Outline each Babesia divergens-infected red blood cell.
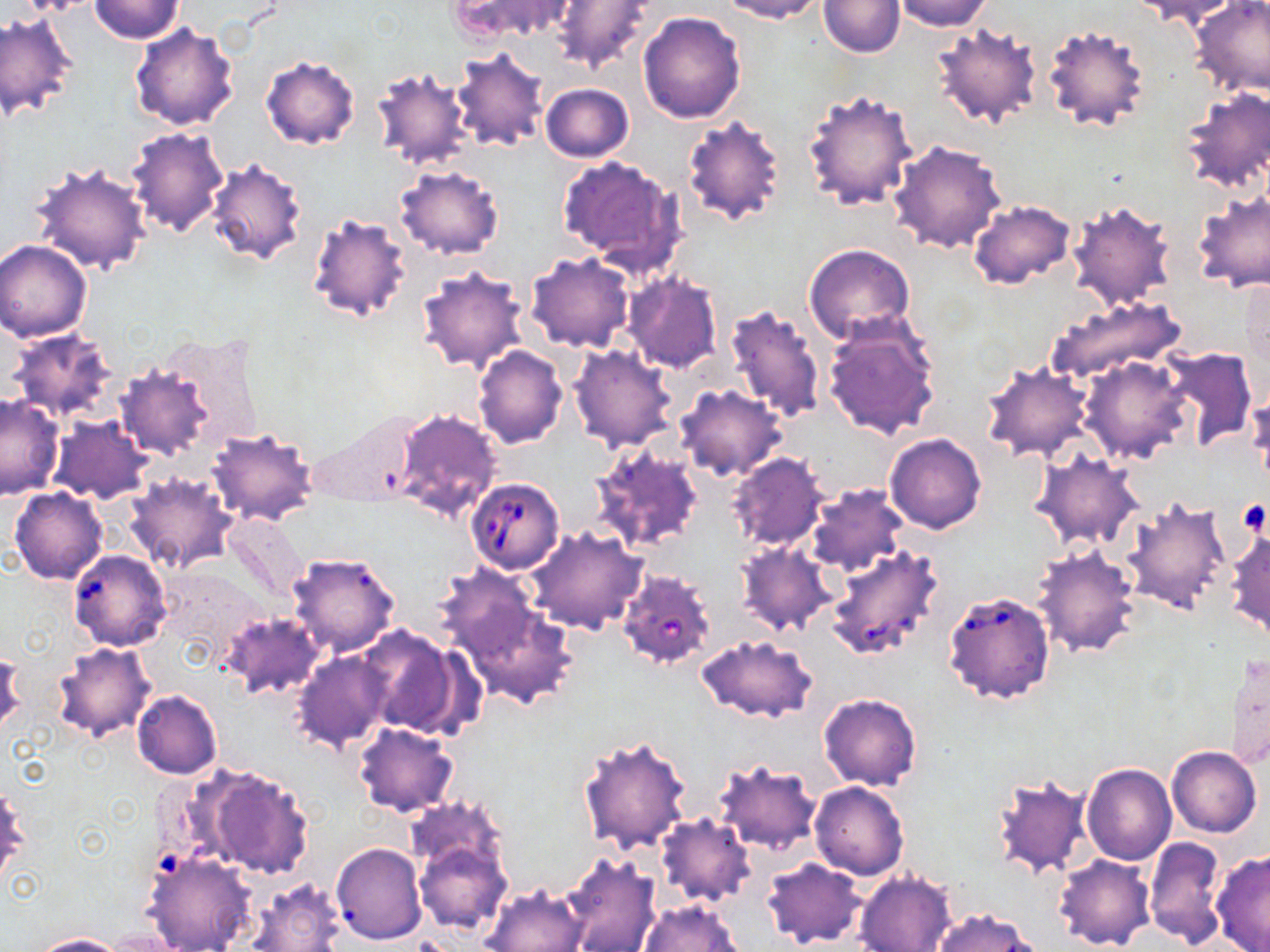

Approximate bounding boxes as (x1, y1, x2, y2) in pixels.
Babesia divergens-infected red blood cells: (465, 478, 565, 574), (826, 545, 943, 661), (71, 552, 172, 653), (616, 569, 716, 671), (944, 589, 1055, 705).

Summary:
  - Uninfected red blood cell locations: (89, 0, 184, 43), (450, 0, 578, 41), (718, 0, 827, 23), (820, 0, 904, 56), (891, 0, 993, 31), (1128, 0, 1241, 26), (1189, 0, 1270, 100), (548, 1, 654, 73), (1, 10, 78, 120), (638, 11, 746, 123), (129, 22, 239, 129), (931, 22, 1043, 130), (1043, 25, 1150, 133), (451, 48, 548, 152), (260, 54, 361, 150), (368, 64, 476, 173), (540, 83, 635, 163), (1180, 87, 1269, 194), (803, 88, 918, 212), (681, 114, 788, 229), (125, 125, 230, 238), (887, 139, 1006, 254), (205, 155, 312, 268), (556, 156, 687, 277), (27, 159, 153, 276), (395, 164, 504, 259), (1191, 188, 1270, 295), (967, 198, 1076, 289), (1066, 199, 1177, 312), (305, 212, 413, 323), (0, 240, 94, 341), (803, 243, 917, 346), (525, 253, 635, 353), (415, 265, 529, 375), (623, 272, 723, 374), (1048, 294, 1187, 386), (724, 303, 826, 425), (820, 315, 942, 442), (6, 327, 118, 423), (568, 344, 678, 452), (472, 346, 568, 449), (1160, 346, 1258, 450), (1080, 355, 1192, 463), (113, 359, 222, 461), (981, 361, 1094, 463), (676, 383, 786, 481), (1246, 387, 1270, 490), (0, 393, 66, 500), (391, 407, 504, 522), (307, 409, 424, 508), (50, 416, 153, 503), (206, 426, 319, 527), (884, 433, 987, 534), (589, 439, 705, 553), (1031, 451, 1143, 550), (727, 453, 828, 550), (124, 472, 237, 573), (804, 483, 907, 578), (10, 487, 107, 584), (1123, 494, 1233, 616), (225, 513, 306, 605), (527, 526, 647, 634), (1227, 528, 1269, 638), (737, 541, 838, 636), (1032, 545, 1141, 657), (286, 551, 401, 658), (447, 581, 579, 709), (221, 610, 323, 701), (357, 626, 470, 739), (696, 634, 818, 723), (50, 641, 156, 744), (1, 650, 25, 738), (1224, 650, 1269, 771), (293, 651, 393, 753), (132, 689, 223, 778), (818, 692, 922, 790), (353, 722, 459, 817), (578, 734, 692, 854), (1166, 745, 1262, 837), (711, 758, 821, 855), (1082, 762, 1177, 865), (200, 767, 314, 879), (989, 773, 1093, 880), (810, 781, 910, 880), (0, 785, 27, 888), (656, 813, 756, 909), (407, 814, 515, 936), (1144, 836, 1227, 947), (331, 843, 426, 944), (141, 848, 256, 952), (1210, 849, 1270, 952), (1055, 853, 1156, 951), (559, 854, 661, 952), (761, 858, 868, 948), (854, 871, 957, 952), (246, 877, 347, 952), (480, 884, 588, 952), (639, 900, 744, 952), (931, 908, 1040, 952), (28, 932, 126, 951)
  - Platelet locations: (1236, 500, 1268, 537)
  - Slide-level diagnosis: Babesia divergens
  - Magnification: 1000x
  - Stain: May-Grünwald-Giemsa
  - Field of view: one of a larger specimen
  - Preparation: thin blood film
  - Modality: optical microscopy
  - Image size: 1270×952 pixels